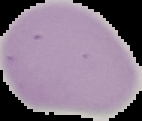
Summary:
  - Image type: cell region segmented out of the field of view; surrounding area masked to black
  - Image size: 142×121 pixels
  - Preparation: thin blood smear
  - Malaria status: uninfected